Assess this cell for malaria.
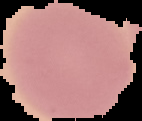
It is uninfected.

image type = segmented cell region with the area outside set to black
preparation = thin blood smear
image size = 142×121 pixels